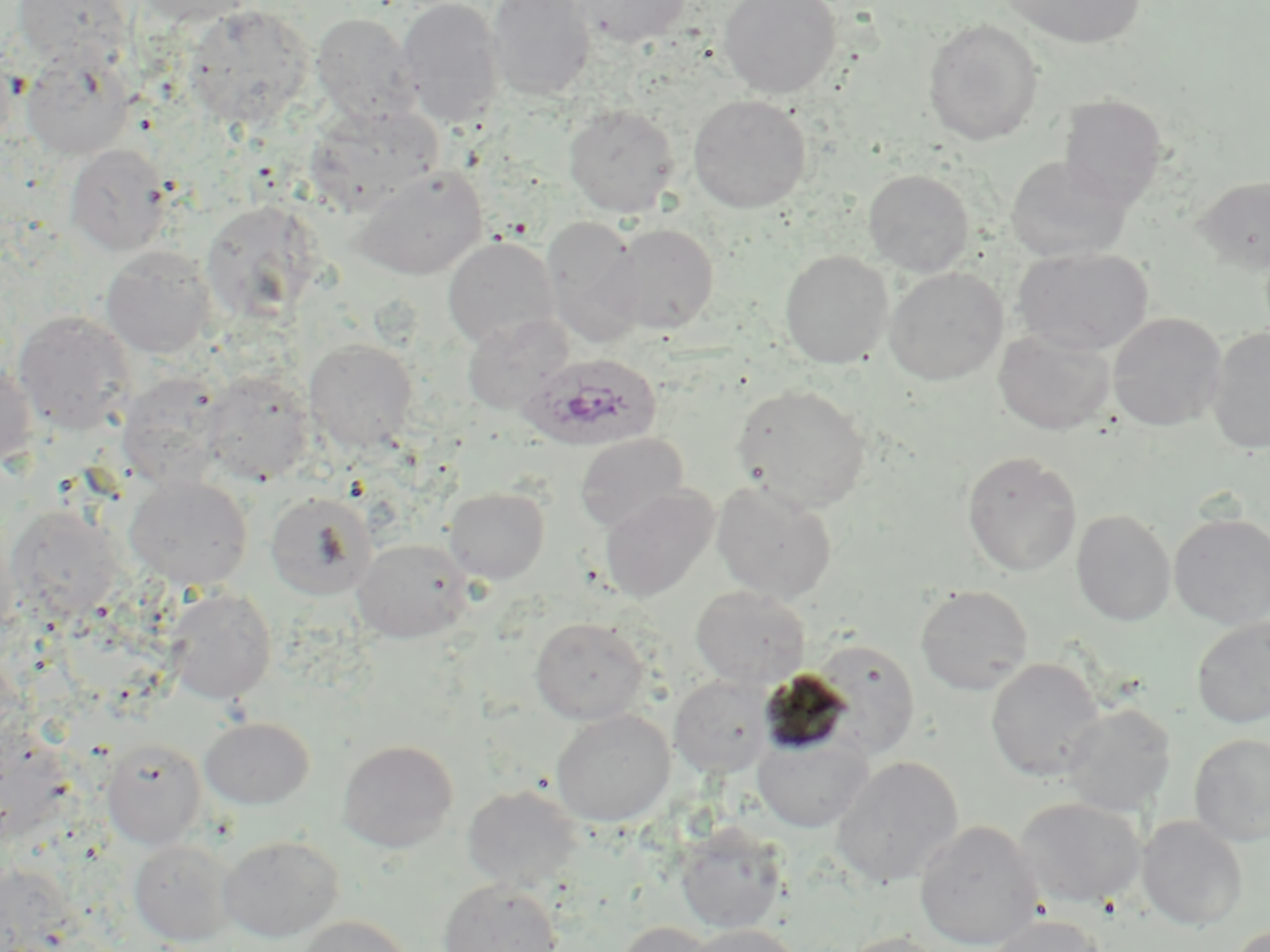 Approximate bounding boxes as [x1, y1, x2, y2] in pixels. Uninfected red blood cell locations: [13, 0, 133, 70], [132, 0, 256, 26], [396, 0, 506, 129], [485, 0, 595, 102], [570, 0, 692, 48], [718, 0, 842, 99], [1004, 0, 1147, 48], [182, 4, 314, 129], [311, 12, 419, 124], [922, 19, 1044, 146], [21, 48, 135, 160], [0, 49, 16, 158], [1057, 94, 1168, 209], [688, 95, 811, 212], [306, 102, 443, 212], [563, 103, 679, 218], [65, 143, 171, 255], [1005, 155, 1132, 262], [352, 166, 487, 280], [863, 169, 974, 276], [1194, 174, 1270, 274], [200, 199, 322, 323], [542, 217, 645, 348], [604, 222, 720, 335], [443, 236, 560, 349], [100, 246, 217, 359], [1013, 247, 1154, 355], [780, 250, 893, 368], [884, 266, 1008, 385], [13, 310, 136, 434], [1108, 312, 1226, 431], [462, 313, 573, 414], [1207, 325, 1270, 454], [993, 329, 1116, 435], [304, 339, 418, 453], [0, 361, 39, 469], [200, 371, 315, 485], [117, 372, 228, 489], [732, 383, 873, 513], [574, 432, 690, 533], [961, 452, 1082, 576], [124, 475, 253, 590], [711, 480, 838, 603], [600, 484, 719, 603], [444, 486, 550, 583], [265, 491, 378, 600], [3, 505, 124, 624], [1071, 509, 1176, 626], [1168, 512, 1269, 628], [351, 537, 473, 642], [915, 584, 1034, 695], [691, 586, 810, 688], [162, 587, 277, 704], [530, 616, 649, 724], [1190, 616, 1270, 729], [809, 638, 920, 758], [985, 657, 1105, 782], [669, 675, 775, 777], [1061, 703, 1177, 816], [550, 709, 675, 826], [200, 717, 314, 809], [752, 732, 873, 832], [1189, 733, 1270, 846], [101, 738, 207, 849], [337, 739, 459, 852], [831, 755, 964, 887], [462, 785, 581, 893], [1015, 798, 1146, 908], [1137, 816, 1247, 931], [914, 819, 1044, 950], [674, 822, 789, 934], [219, 835, 343, 942], [129, 840, 237, 945], [438, 879, 563, 952], [981, 914, 1111, 952], [296, 915, 415, 952], [617, 921, 720, 952], [1228, 922, 1269, 951], [684, 924, 805, 952], [839, 932, 951, 952]. Plasmodium ovale-infected red blood cell locations: [520, 353, 662, 451]. Slide-level diagnosis: Plasmodium ovale. May-Grünwald-Giemsa stain. Image is 1270×952 pixels. Thin blood smear. Optical microscopy. 1000x magnification. One field of a larger specimen.